Comment on the morphology of the red blood cells.
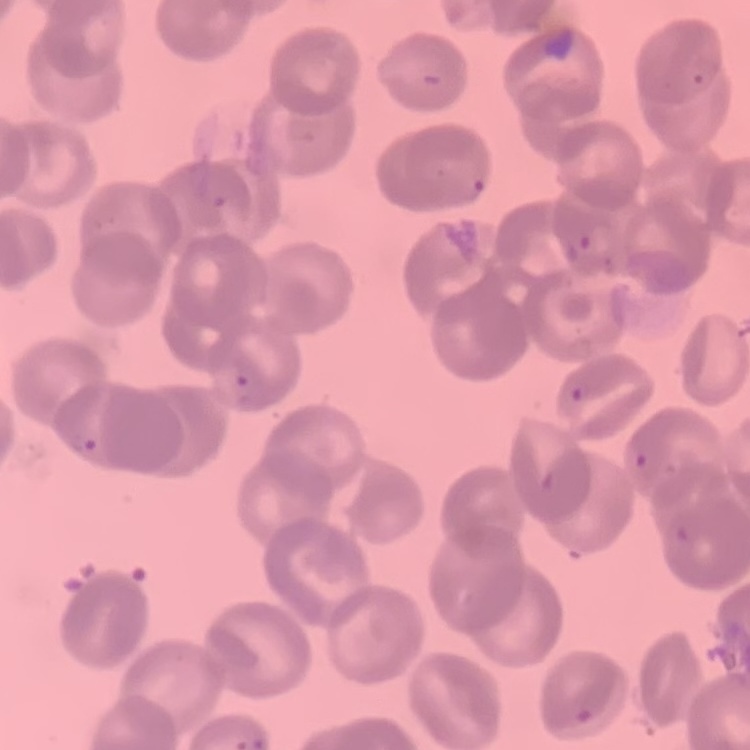

They show rouleaux formation.

stain = Field's or Giemsa
image type = square crop of a larger photomicrograph
preparation = thin blood film